Identify the preparation type.
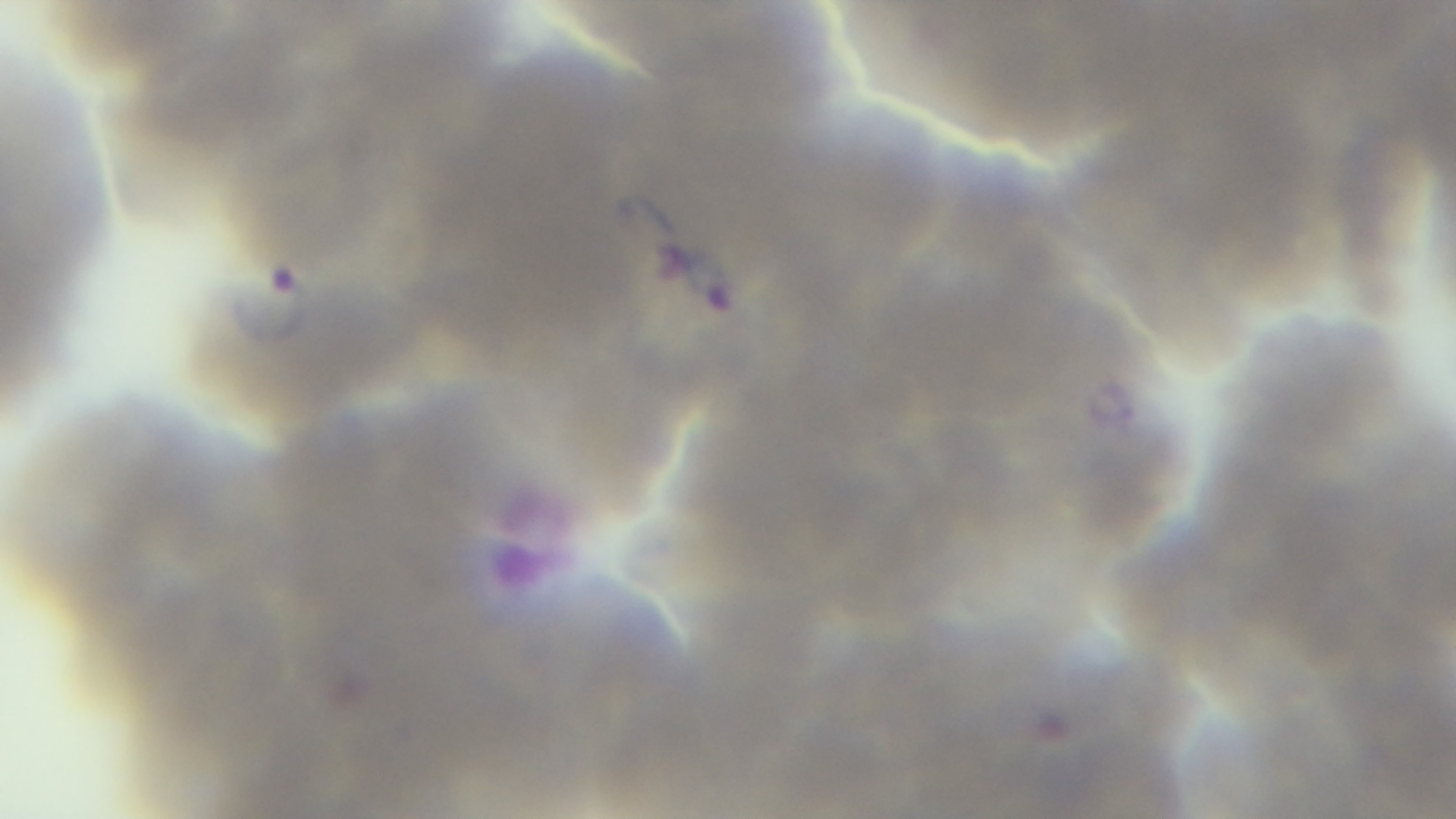

A thin smear.

Malaria status: infected. One field from the slide. Captured with a mounted 4K digital camera. Giemsa stain. 100x oil-immersion objective. Light microscopy.